Assess this cell for malaria.
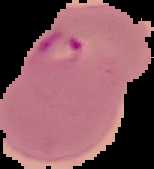
It is parasitized.

From a thin blood film. Image is 154×169 pixels. The area outside the segmented cell region is set to black.